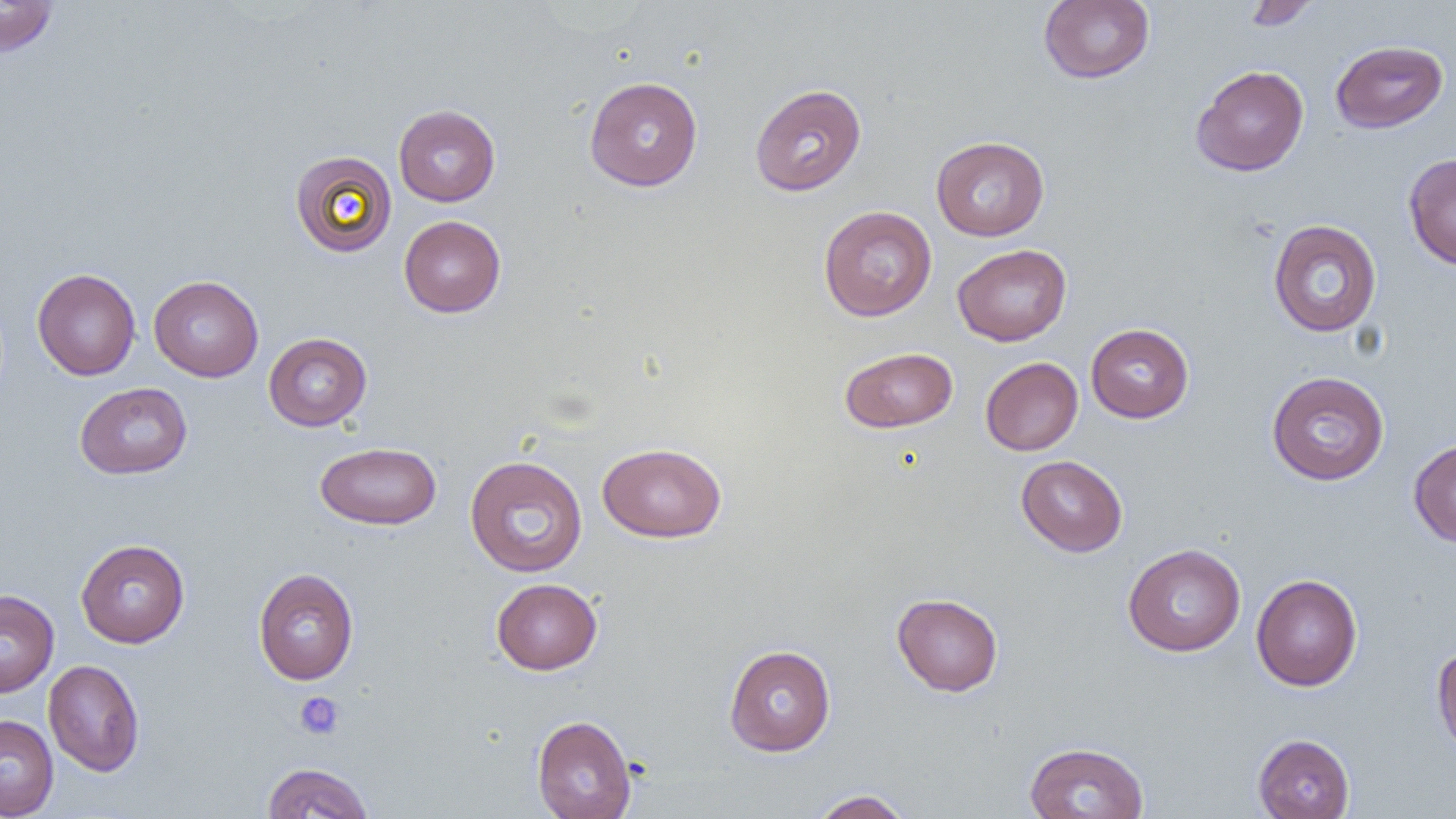
slide-level diagnosis = negative for blood parasites
magnification = 1000x
platelet locations = approximate bounding boxes as (x1, y1, x2, y2) in pixels: (294, 692, 345, 739)
preparation = thin blood smear
uninfected red blood cell locations = approximate bounding boxes as (x1, y1, x2, y2) in pixels: (1039, 0, 1154, 84), (1241, 0, 1321, 31), (0, 1, 58, 57), (1331, 39, 1448, 134), (1191, 65, 1309, 177), (584, 76, 703, 191), (749, 83, 867, 196), (393, 104, 501, 207), (931, 135, 1049, 241), (941, 136, 1056, 347), (290, 150, 397, 257), (1403, 152, 1456, 270), (818, 205, 937, 321), (398, 215, 506, 317), (1267, 219, 1382, 338), (953, 243, 1072, 346), (32, 268, 141, 381), (148, 275, 264, 381), (1085, 323, 1194, 423), (263, 332, 372, 431), (840, 346, 958, 433), (980, 357, 1083, 455), (1266, 370, 1390, 486), (74, 382, 192, 479), (1408, 439, 1456, 547), (314, 441, 442, 530), (597, 442, 727, 543), (465, 455, 588, 577), (1016, 455, 1128, 557), (75, 539, 190, 648), (1122, 543, 1246, 656), (253, 567, 359, 685), (1251, 574, 1362, 691), (491, 578, 602, 675), (0, 589, 59, 697), (892, 593, 1003, 696), (723, 644, 836, 756), (1431, 644, 1456, 759), (43, 659, 145, 777), (0, 714, 58, 819), (532, 714, 636, 819), (1253, 733, 1355, 819), (1024, 741, 1149, 819), (261, 762, 374, 818), (810, 789, 913, 818)
image size = 1456×819 pixels
field of view = single
modality = light microscopy